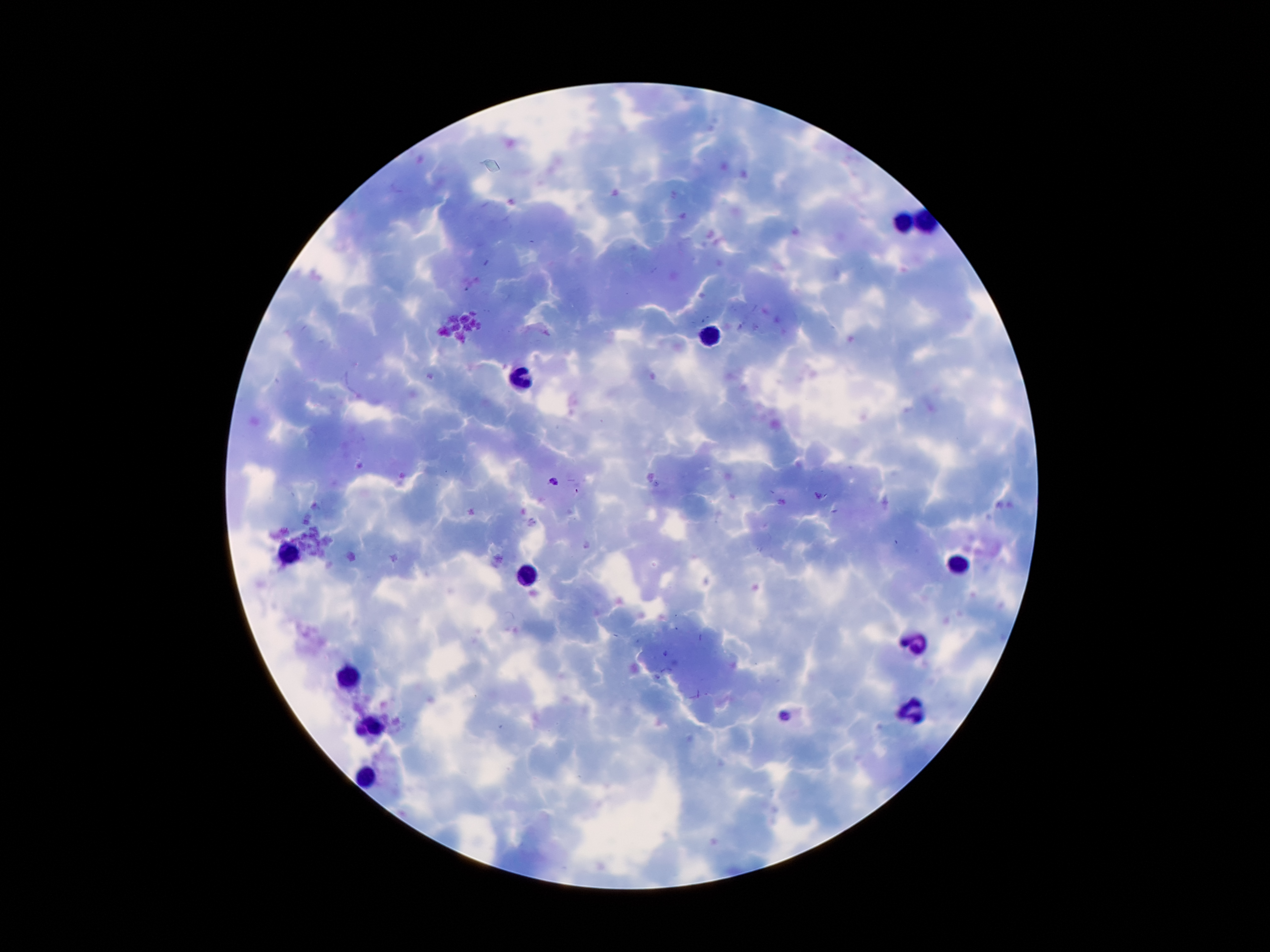
Approximate centers as {x, y} in pixels.
Summary:
  - Malaria parasite locations: {554, 481}, {783, 714}
  - Leukocyte locations: {901, 223}, {713, 335}, {523, 379}, {287, 555}, {957, 567}, {525, 577}, {915, 645}, {347, 677}, {919, 715}, {375, 725}, {367, 779}
  - Magnification: 100x
  - Capture: smartphone through the microscope eyepiece
  - Patient malaria status: positive for Plasmodium falciparum
  - Preparation: thick blood film
  - Stain: Giemsa
  - Image size: 1270×952 pixels
  - Field of view: one from this slide